Report the malaria status of this cell.
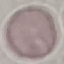
It is uninfected.

Summary:
  - Capture: smartphone through the microscope eyepiece
  - Stain: Giemsa
  - Preparation: thin smear
  - Image type: automatically extracted cell patch, resized to 64 × 64 pixels